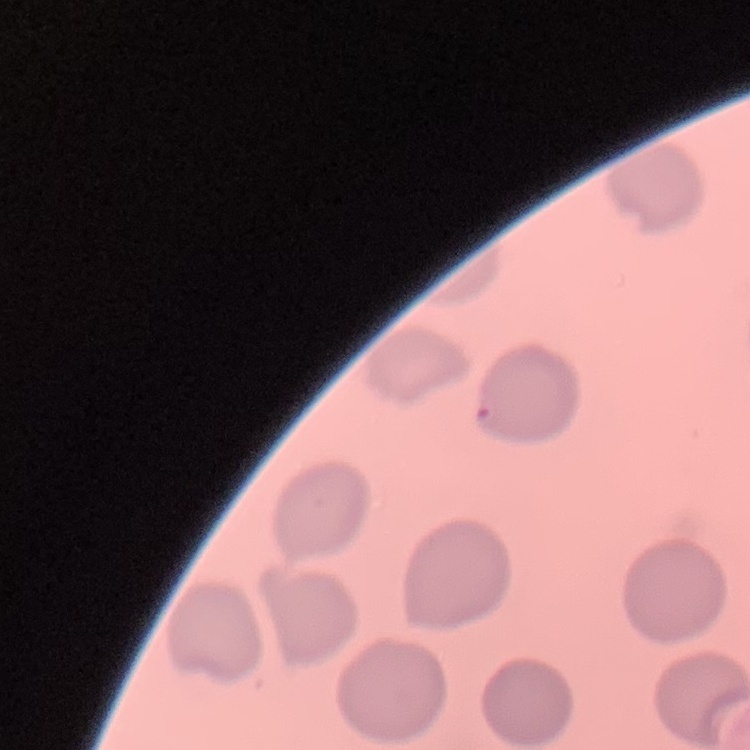
red_blood_cell_morphology: no rouleaux formation
stain: Field's or Giemsa
image_type: one tile cut from a larger photomicrograph
preparation: thin peripheral smear